Report the malaria status of this cell.
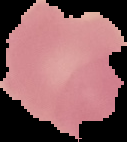

It is uninfected.

From a thin blood film. Image is 127×142 pixels. Segmented cell region on a black background.